Assess for malaria.
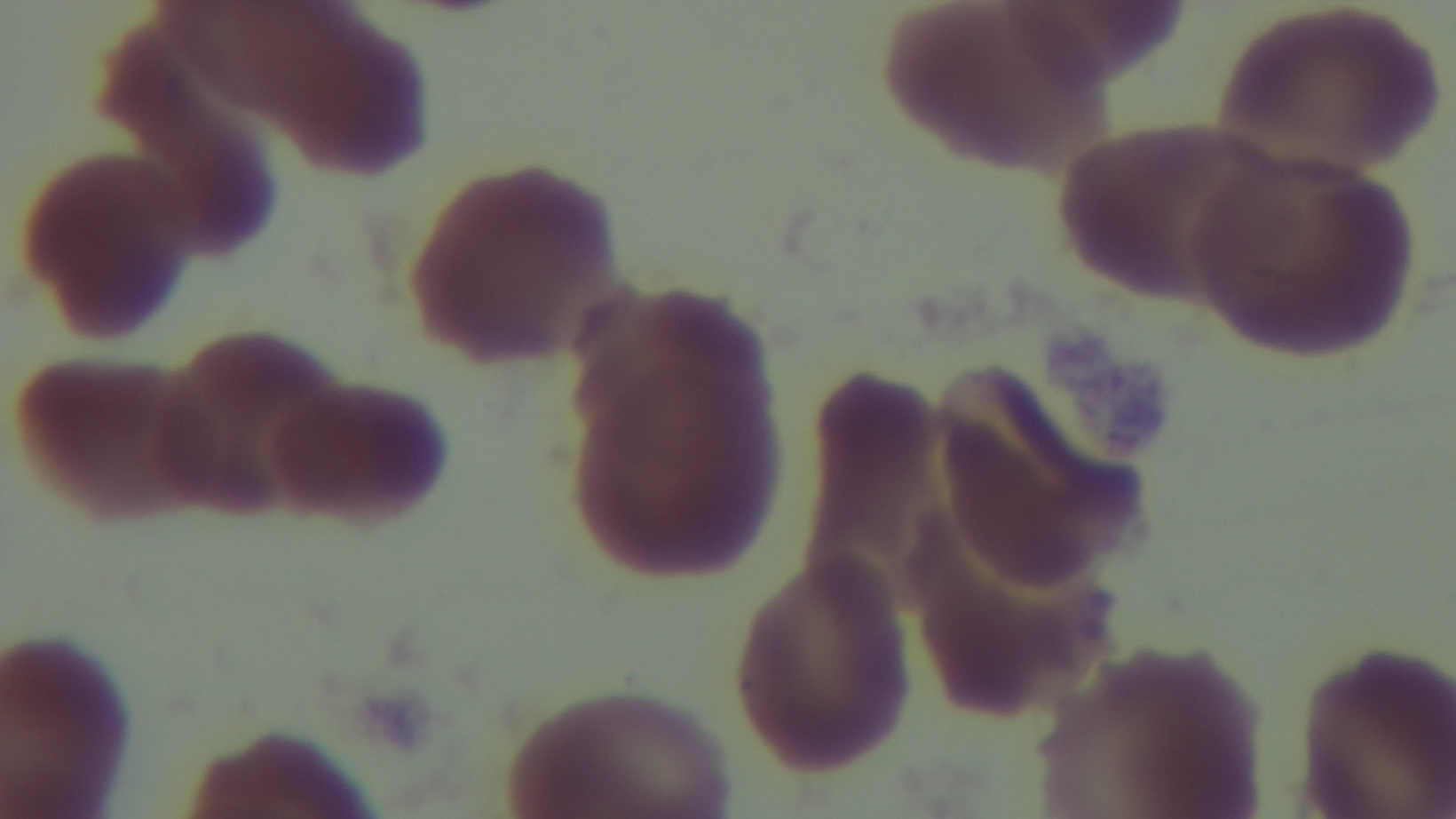

Uninfected.

Summary:
  - Field of view: one from the slide
  - Stain: Giemsa
  - Modality: light microscopy
  - Capture: mounted 4K digital camera
  - Objective: 100x oil immersion
  - Preparation: thin